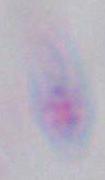
Summary:
  - Magnification: 1000x
  - Identification: Toxoplasma gondii
  - Modality: photomicrograph